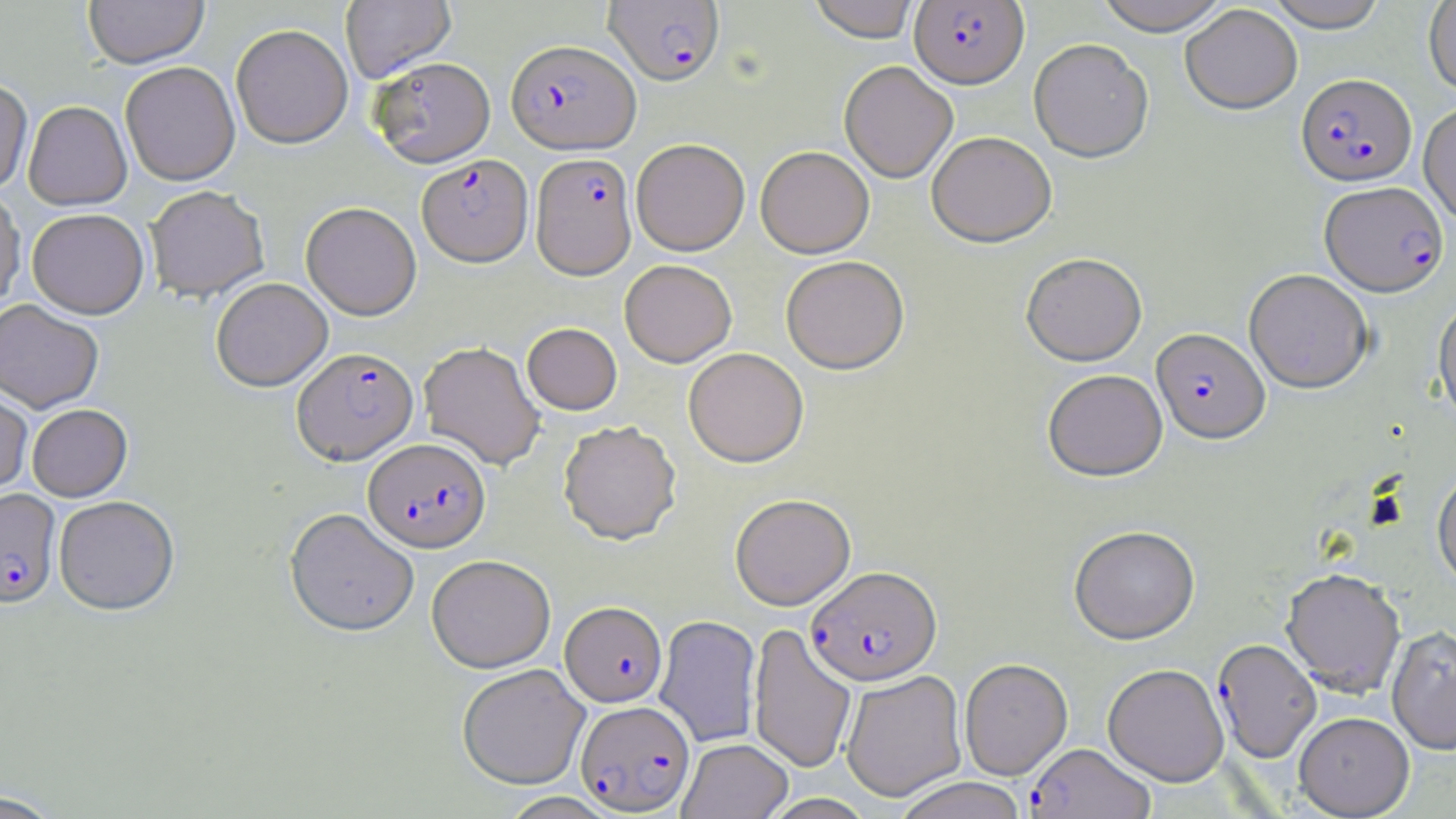
{
  "slide_level_diagnosis": "Plasmodium falciparum",
  "field_of_view": "single",
  "uninfected_red_blood_cell_locations": "approximate bounding boxes as named x1/y1/x2/y2 corners in pixels: (x1=83, y1=0, x2=209, y2=69), (x1=340, y1=0, x2=456, y2=82), (x1=807, y1=0, x2=921, y2=42), (x1=1095, y1=0, x2=1231, y2=35), (x1=1265, y1=0, x2=1389, y2=32), (x1=1423, y1=2, x2=1456, y2=96), (x1=1180, y1=4, x2=1302, y2=114), (x1=231, y1=24, x2=353, y2=149), (x1=1029, y1=38, x2=1154, y2=162), (x1=369, y1=56, x2=496, y2=168), (x1=839, y1=60, x2=958, y2=183), (x1=120, y1=61, x2=240, y2=186), (x1=0, y1=78, x2=33, y2=194), (x1=23, y1=101, x2=132, y2=211), (x1=1418, y1=102, x2=1456, y2=225), (x1=926, y1=131, x2=1056, y2=248), (x1=631, y1=139, x2=749, y2=256), (x1=755, y1=147, x2=874, y2=259), (x1=144, y1=185, x2=269, y2=303), (x1=0, y1=187, x2=25, y2=311), (x1=300, y1=202, x2=421, y2=320), (x1=27, y1=208, x2=149, y2=319), (x1=1021, y1=253, x2=1147, y2=367), (x1=781, y1=257, x2=910, y2=376), (x1=620, y1=260, x2=737, y2=367), (x1=1244, y1=269, x2=1373, y2=393), (x1=210, y1=277, x2=333, y2=392), (x1=1433, y1=296, x2=1456, y2=431), (x1=0, y1=299, x2=104, y2=413), (x1=522, y1=323, x2=622, y2=415), (x1=419, y1=341, x2=545, y2=471), (x1=683, y1=348, x2=809, y2=468), (x1=1042, y1=369, x2=1168, y2=482), (x1=0, y1=384, x2=33, y2=495), (x1=27, y1=404, x2=132, y2=501), (x1=558, y1=421, x2=682, y2=545), (x1=1433, y1=465, x2=1456, y2=591), (x1=730, y1=493, x2=856, y2=610), (x1=53, y1=495, x2=179, y2=615), (x1=284, y1=508, x2=419, y2=638), (x1=1069, y1=525, x2=1200, y2=645), (x1=427, y1=555, x2=556, y2=673), (x1=1281, y1=570, x2=1406, y2=699), (x1=655, y1=615, x2=761, y2=747), (x1=749, y1=624, x2=857, y2=773), (x1=1387, y1=626, x2=1456, y2=756), (x1=959, y1=658, x2=1073, y2=780), (x1=457, y1=664, x2=590, y2=789), (x1=1102, y1=664, x2=1229, y2=787), (x1=841, y1=670, x2=966, y2=802), (x1=1294, y1=713, x2=1415, y2=818), (x1=678, y1=738, x2=792, y2=819), (x1=892, y1=777, x2=1029, y2=819), (x1=0, y1=790, x2=64, y2=818), (x1=759, y1=793, x2=877, y2=819)",
  "preparation": "thin blood smear",
  "plasmodium_falciparum_infected_red_blood_cell_locations": "approximate bounding boxes as named x1/y1/x2/y2 corners in pixels: (x1=604, y1=1, x2=724, y2=86), (x1=909, y1=1, x2=1028, y2=88), (x1=506, y1=39, x2=640, y2=154), (x1=1296, y1=73, x2=1417, y2=186), (x1=531, y1=153, x2=637, y2=280), (x1=417, y1=154, x2=533, y2=267), (x1=1320, y1=181, x2=1448, y2=296), (x1=1151, y1=328, x2=1270, y2=446), (x1=292, y1=347, x2=418, y2=465), (x1=363, y1=438, x2=491, y2=553), (x1=0, y1=488, x2=61, y2=608), (x1=806, y1=565, x2=942, y2=686), (x1=560, y1=602, x2=667, y2=707), (x1=1217, y1=645, x2=1326, y2=769), (x1=575, y1=700, x2=695, y2=815), (x1=1026, y1=743, x2=1155, y2=819)",
  "stain": "May-Grünwald-Giemsa",
  "magnification": "1000x",
  "image_size": "1456×819 pixels",
  "modality": "light microscopy"
}